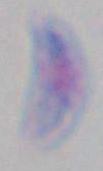

magnification = 1000x
identification = Toxoplasma gondii
modality = micrograph